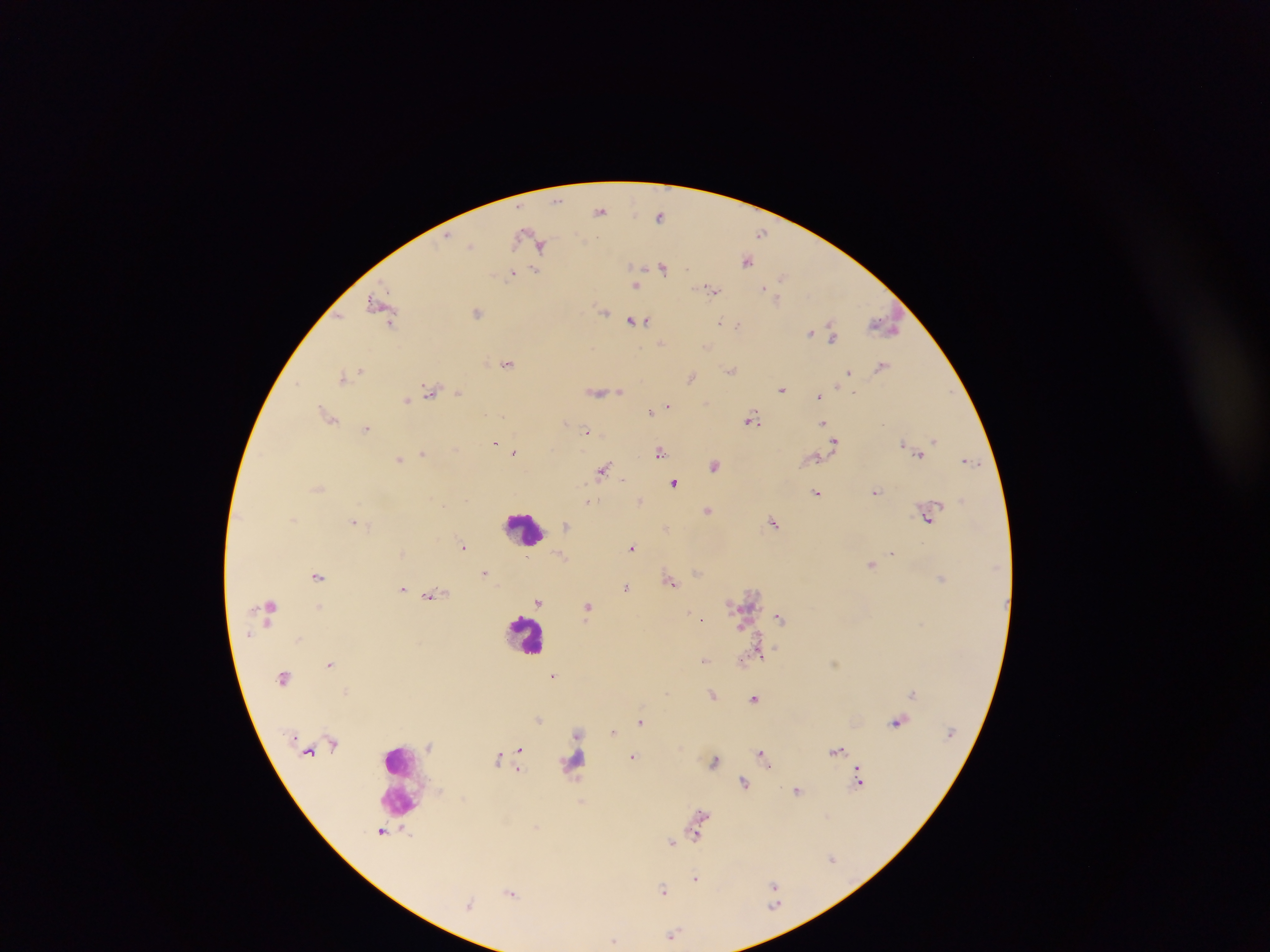
Approximate centers as {x, y} in pixels. Leukocyte locations: {525, 530}, {527, 635}, {575, 760}, {404, 781}. Plasmodium parasite locations: {557, 200}, {601, 209}, {661, 216}, {763, 231}, {531, 241}, {539, 244}, {471, 246}, {747, 260}, {663, 266}, {537, 269}, {513, 272}, {783, 276}, {636, 284}, {711, 289}, {775, 296}, {382, 305}, {477, 311}, {604, 311}, {635, 321}, {720, 321}, {738, 325}, {884, 325}, {811, 332}, {832, 332}, {661, 343}, {706, 345}, {508, 362}, {882, 365}, {731, 369}, {848, 372}, {345, 376}, {691, 377}, {782, 388}, {432, 391}, {619, 391}, {458, 392}, {598, 392}, {820, 395}, {406, 399}, {668, 406}, {652, 411}, {329, 415}, {752, 418}, {823, 422}, {367, 427}, {588, 431}, {835, 440}, {495, 441}, {934, 441}, {903, 444}, {514, 451}, {661, 451}, {422, 453}, {919, 453}, {400, 457}, {815, 457}, {971, 460}, {715, 464}, {603, 469}, {675, 482}, {318, 487}, {877, 491}, {818, 492}, {640, 500}, {588, 502}, {709, 510}, {929, 516}, {355, 520}, {774, 521}, {567, 526}, {666, 529}, {463, 546}, {633, 547}, {892, 552}, {403, 553}, {561, 555}, {872, 564}, {486, 573}, {318, 575}, {942, 578}, {671, 580}, {626, 587}, {403, 589}, {431, 594}, {539, 602}, {319, 606}, {588, 606}, {780, 617}, {702, 618}, {744, 625}, {759, 649}, {705, 660}, {330, 662}, {554, 675}, {347, 691}, {913, 693}, {713, 694}, {755, 698}, {538, 719}, {641, 720}, {899, 720}, {614, 732}, {577, 733}, {431, 746}, {519, 749}, {838, 750}, {763, 753}, {633, 756}, {499, 757}, {715, 759}, {519, 767}, {860, 777}, {745, 782}, {798, 789}, {581, 801}, {702, 814}, {537, 828}, {383, 830}, {696, 834}, {672, 841}, {833, 858}, {696, 878}, {775, 885}, {663, 889}, {511, 892}, {775, 904}, {673, 934}, {614, 941}. Sample from Ghana. Image is 1270×952 pixels. Thick blood smear. One field of view. Photographed through a microscope with a mobile-phone camera.